Give the position of every leukocyte visible.
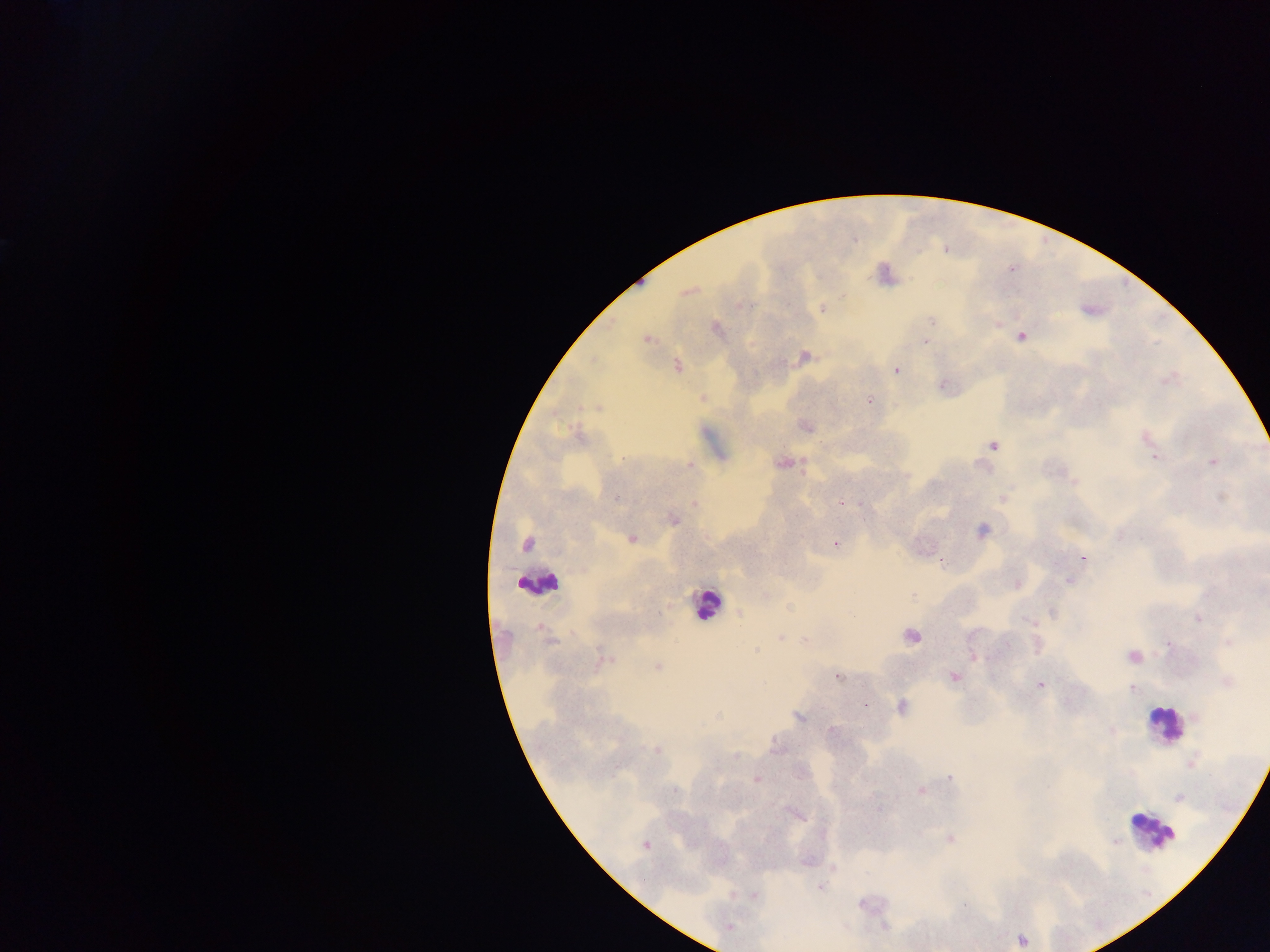
Approximate centers as x y in pixels.
Leukocytes: 540 582; 706 603; 1163 724; 1151 830.

{
  "image_size": "1270×952 pixels",
  "country": "Ghana",
  "malaria_parasite_locations": "approximate centers as x y in pixels: 1011 269; 687 292; 822 309; 932 320; 716 328; 1020 336; 646 339; 924 341; 804 357; 677 366; 896 370; 1168 380; 942 385; 702 397; 869 400; 598 408; 807 427; 578 435; 1147 438; 993 445; 1150 447; 1155 457; 622 459; 804 462; 1212 462; 781 463; 689 465; 1075 483; 1221 497; 616 498; 1002 499; 695 503; 841 503; 673 520; 981 530; 631 539; 526 544; 835 544; 1083 558; 941 562; 1067 581; 1017 585; 1052 611; 740 614; 1199 618; 1028 620; 540 627; 780 637; 911 637; 549 641; 806 641; 1228 642; 1007 644; 1168 644; 756 651; 974 657; 1133 657; 604 660; 657 667; 838 677; 954 677; 1227 683; 1041 684; 1132 688; 864 704; 902 707; 718 716; 798 717; 832 731; 1112 731; 775 747; 657 750; 736 755; 1192 762; 950 777; 757 778; 921 791; 1178 797; 796 813; 950 839; 1114 841; 646 845; 820 887; 754 895; 861 904; 964 905; 729 927; 1021 940",
  "preparation": "thick blood film",
  "field_of_view": "single",
  "capture": "mobile-phone photograph through a microscope"
}